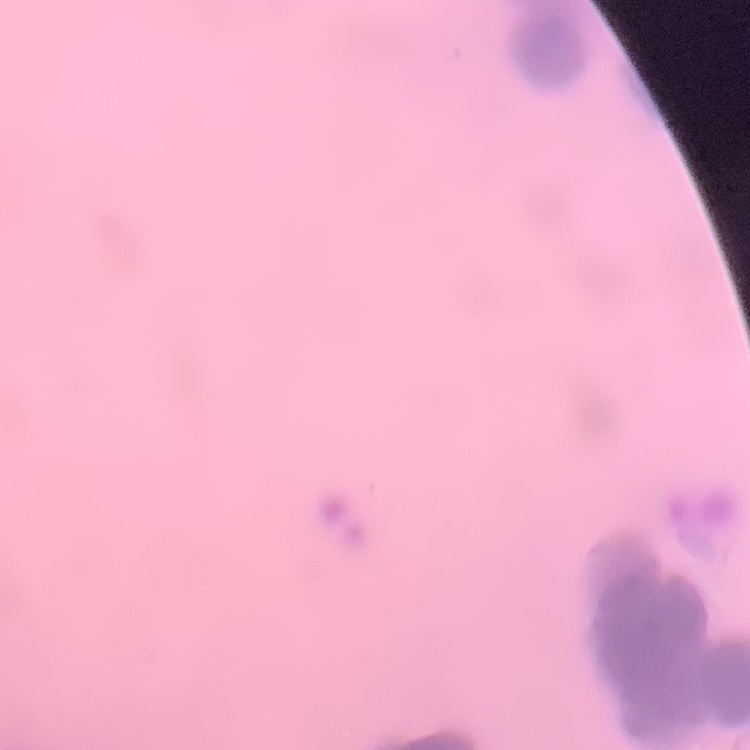

Summary:
  - Red blood cell morphology: rouleaux formation
  - Image type: square crop of a larger photomicrograph
  - Stain: Field's or Giemsa
  - Preparation: thin peripheral smear